Describe the morphology of the red blood cells.
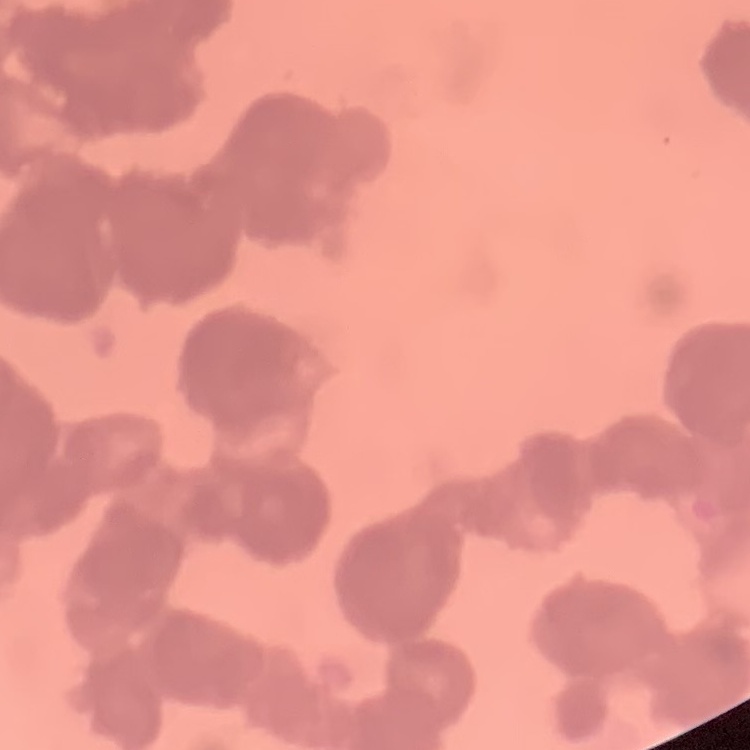
Rouleaux formation.

Stained with either Field's or Giemsa. Thin peripheral smear. One tile cut from a larger photomicrograph.